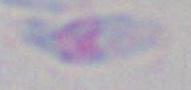
{
  "identification": "Toxoplasma gondii",
  "magnification": "1000x",
  "modality": "photomicrograph"
}